Give the extent of the Plasmodium falciparum parasites you find, grouped by life-cycle stage — ring form, trophozoite, schizont, or gametocyte.
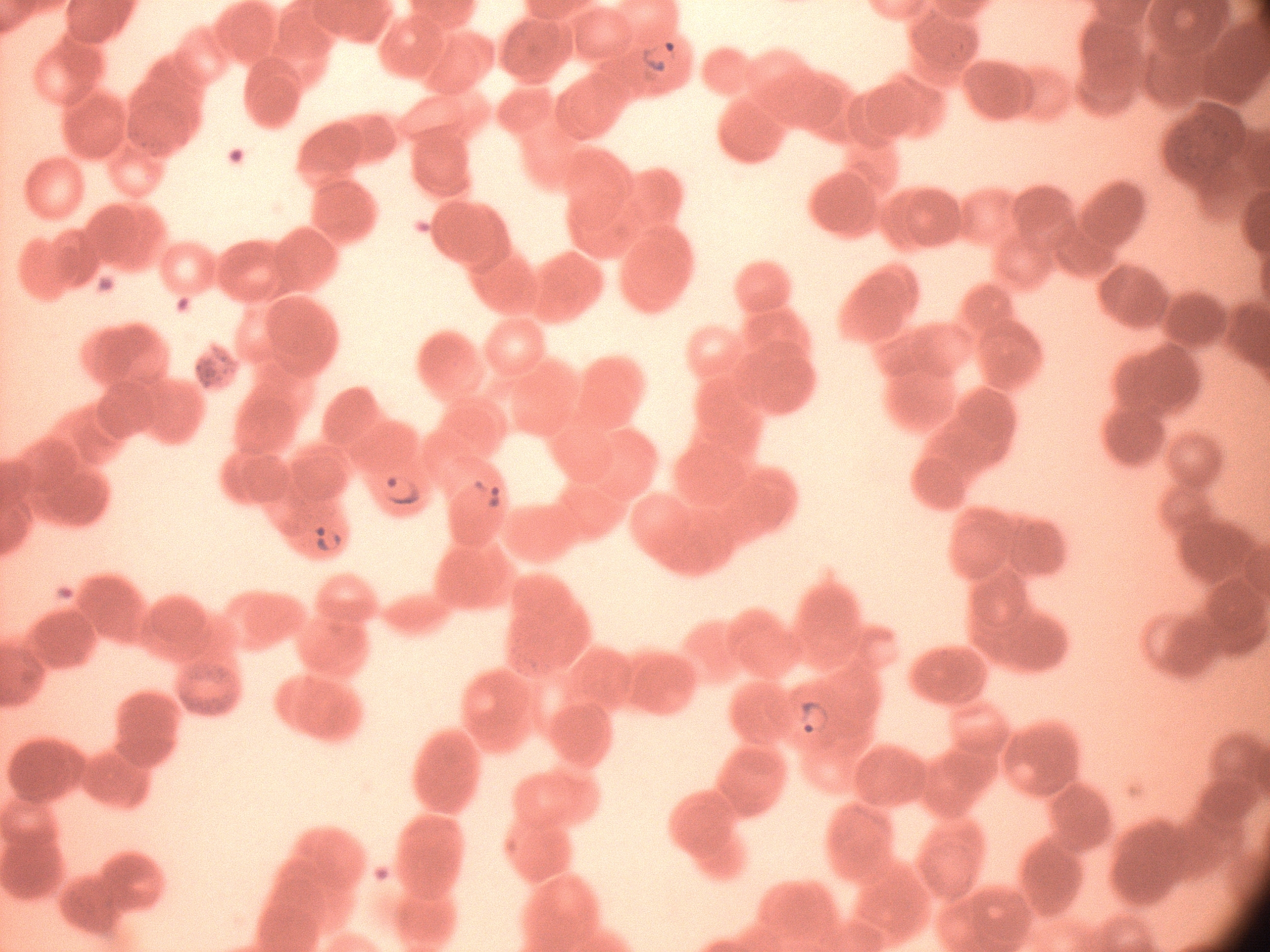

Approximate bounding boxes as [x1, y1, x2, y2] in pixels, from the source annotation, which is not necessarily exhaustive.
Ring forms: [634, 37, 682, 81], [372, 468, 425, 517], [462, 468, 507, 516], [305, 516, 347, 561], [786, 693, 837, 742].

Species: Plasmodium falciparum. Leica DM2000 optical microscope with a built-in camera. Image is 1270×952 pixels. Giemsa-stained preparation. Single field of view. Thin blood film. 100x magnification.